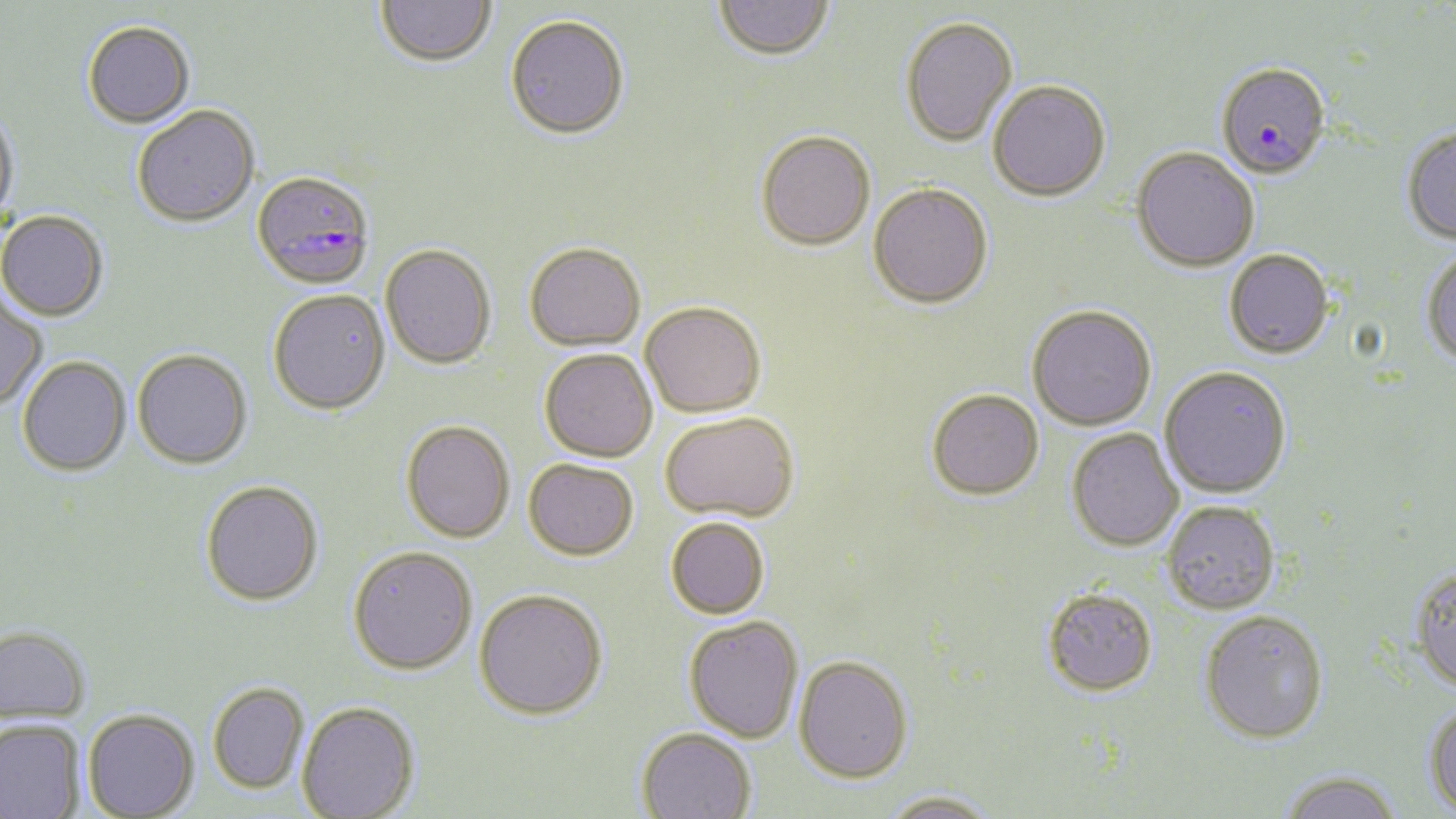
slide-level diagnosis = Plasmodium falciparum
uninfected red blood cell locations = approximate bounding boxes as (x1, y1, x2, y2) in pixels: (376, 0, 497, 68), (713, 0, 835, 62), (506, 16, 631, 140), (900, 17, 1018, 147), (83, 22, 195, 129), (988, 80, 1112, 202), (0, 104, 19, 230), (132, 106, 260, 228), (1402, 127, 1456, 246), (756, 131, 876, 250), (1131, 147, 1259, 273), (868, 183, 994, 308), (0, 210, 109, 321), (524, 242, 646, 350), (380, 244, 496, 369), (1421, 248, 1456, 372), (1224, 250, 1334, 360), (268, 289, 390, 414), (0, 292, 47, 410), (640, 302, 766, 418), (1026, 305, 1156, 431), (539, 348, 657, 461), (132, 349, 252, 469), (17, 356, 131, 476), (1160, 366, 1292, 499), (927, 388, 1044, 499), (660, 411, 799, 522), (401, 420, 515, 542), (1066, 428, 1185, 553), (523, 458, 639, 559), (200, 480, 323, 605), (1162, 501, 1280, 614), (665, 517, 770, 618), (348, 545, 478, 673), (1410, 567, 1456, 697), (1042, 587, 1158, 696), (474, 588, 608, 719), (1200, 610, 1329, 744), (684, 615, 804, 742), (0, 624, 92, 723), (794, 655, 914, 782), (208, 681, 309, 793), (297, 700, 421, 819), (1424, 701, 1456, 817), (83, 708, 200, 818), (0, 718, 85, 819), (637, 727, 756, 819), (1278, 772, 1405, 819), (878, 791, 1002, 819)
field of view = single
stain = May-Grünwald-Giemsa
magnification = 1000x
modality = optical microscopy
preparation = thin blood smear
image size = 1456×819 pixels
Plasmodium falciparum-infected red blood cell locations = approximate bounding boxes as (x1, y1, x2, y2) in pixels: (1216, 63, 1330, 180), (253, 171, 374, 291)